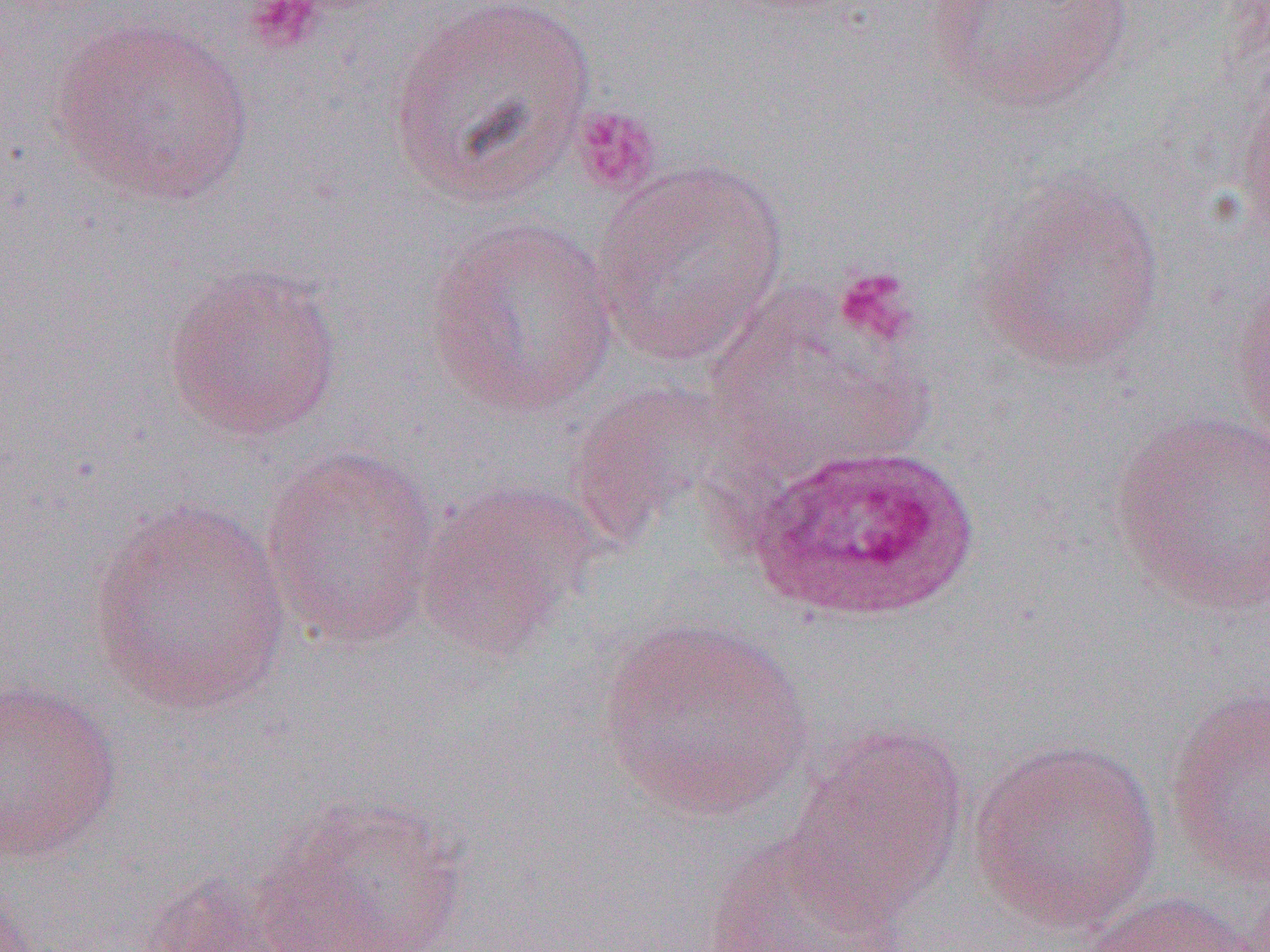

Plasmodium ovale-infected red blood cell locations = approximate bounding boxes as (x1, y1, x2, y2) in pixels: (743, 441, 982, 624)
slide-level diagnosis = Plasmodium ovale
preparation = thin blood film
field of view = single
magnification = 1000x
uninfected red blood cell locations = approximate bounding boxes as (x1, y1, x2, y2) in pixels: (385, 0, 596, 209), (925, 0, 1134, 112), (49, 14, 256, 206), (1236, 78, 1270, 247), (592, 160, 790, 367), (970, 172, 1169, 376), (423, 216, 621, 420), (164, 263, 345, 441), (1231, 274, 1270, 446), (703, 288, 927, 480), (565, 380, 744, 546), (1105, 409, 1270, 616), (261, 446, 442, 649), (413, 478, 604, 658), (88, 496, 295, 717), (598, 616, 813, 821), (0, 679, 124, 863), (1165, 683, 1270, 887), (782, 722, 968, 927), (968, 738, 1163, 933), (256, 795, 468, 952), (701, 834, 918, 952), (136, 871, 302, 952), (1074, 890, 1265, 952)
platelet locations = approximate bounding boxes as (x1, y1, x2, y2) in pixels: (244, 0, 324, 55), (571, 105, 663, 196), (831, 265, 920, 348)
image size = 1270×952 pixels
modality = optical microscopy